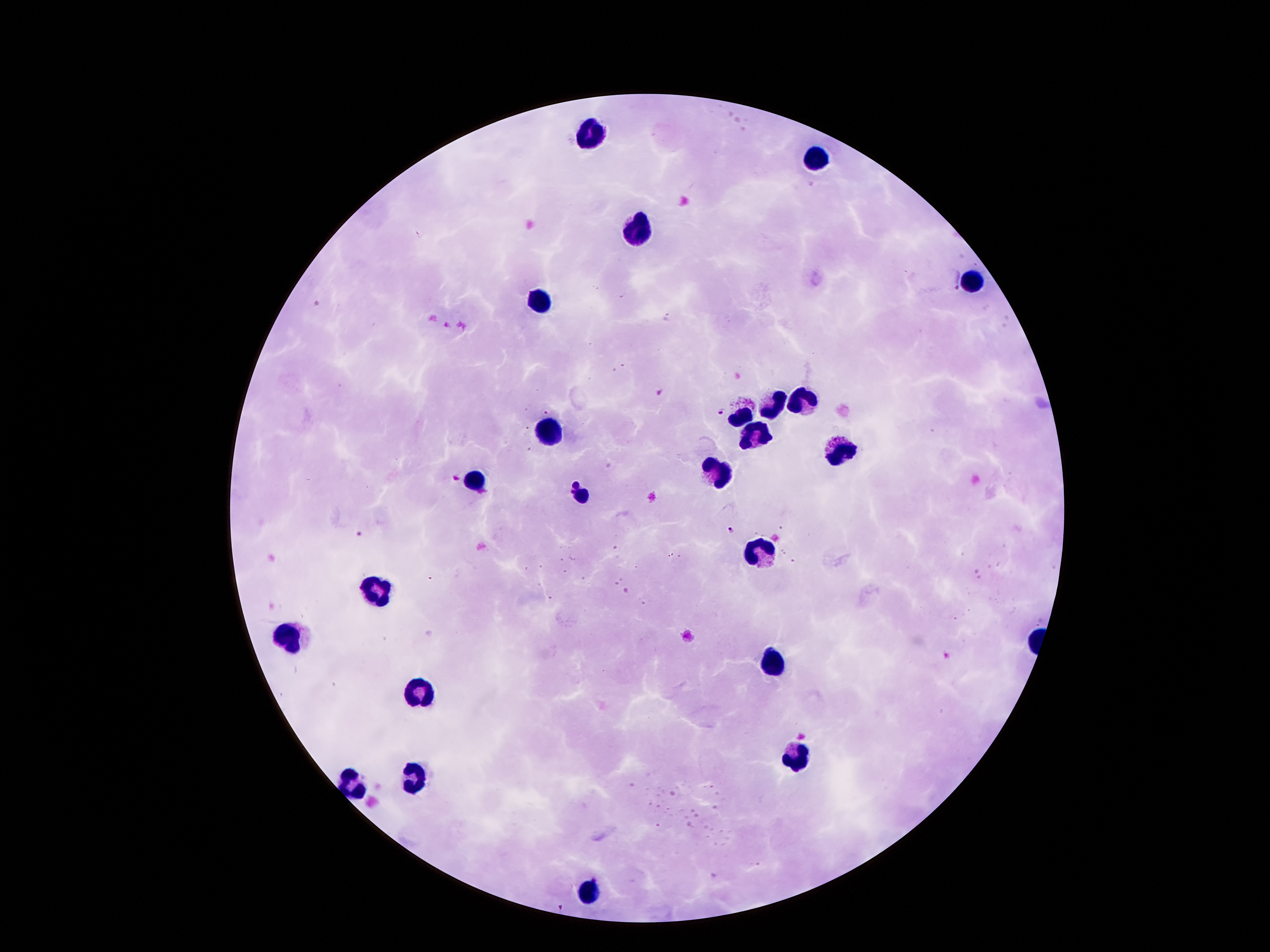
Approximate centers as [x, y] in pixels. Plasmodium parasite locations: [945, 279], [660, 393], [722, 411], [731, 530], [358, 533]. Leukocyte locations: [587, 130], [817, 159], [635, 232], [971, 282], [538, 300], [801, 400], [769, 402], [739, 416], [547, 429], [758, 436], [839, 450], [717, 472], [476, 480], [581, 495], [756, 554], [376, 589], [287, 639], [773, 666], [417, 693], [798, 757], [410, 775], [354, 782], [587, 895]. Giemsa-stained preparation. Patient malaria status: infected with Plasmodium falciparum. Image is 1270×952 pixels. Thick blood film. One field from this slide. 100x magnification. Smartphone photograph taken through the microscope eyepiece.